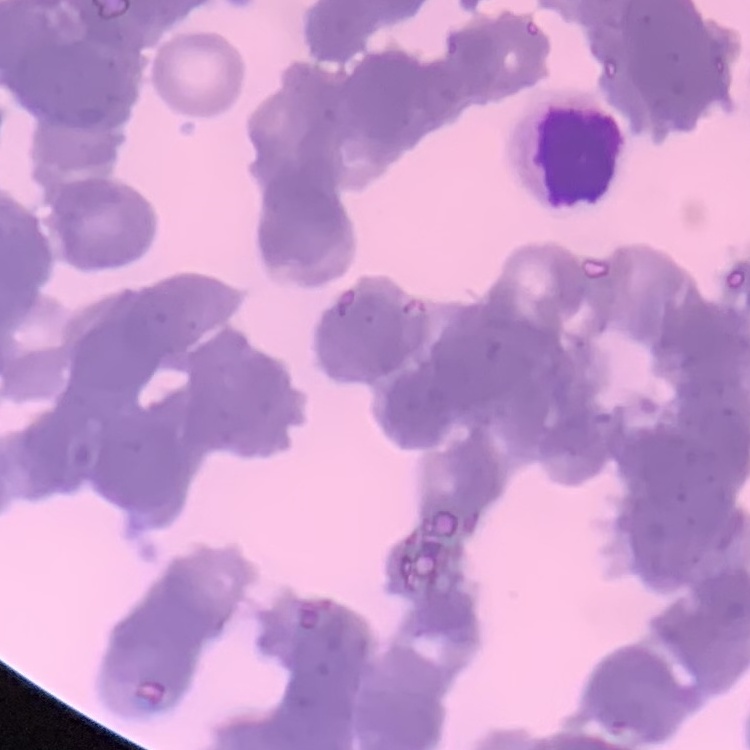

Summary:
  - Erythrocyte morphology: rouleaux formation
  - Stain: Field's or Giemsa
  - Image type: one tile cut from a larger photomicrograph
  - Preparation: thin peripheral smear